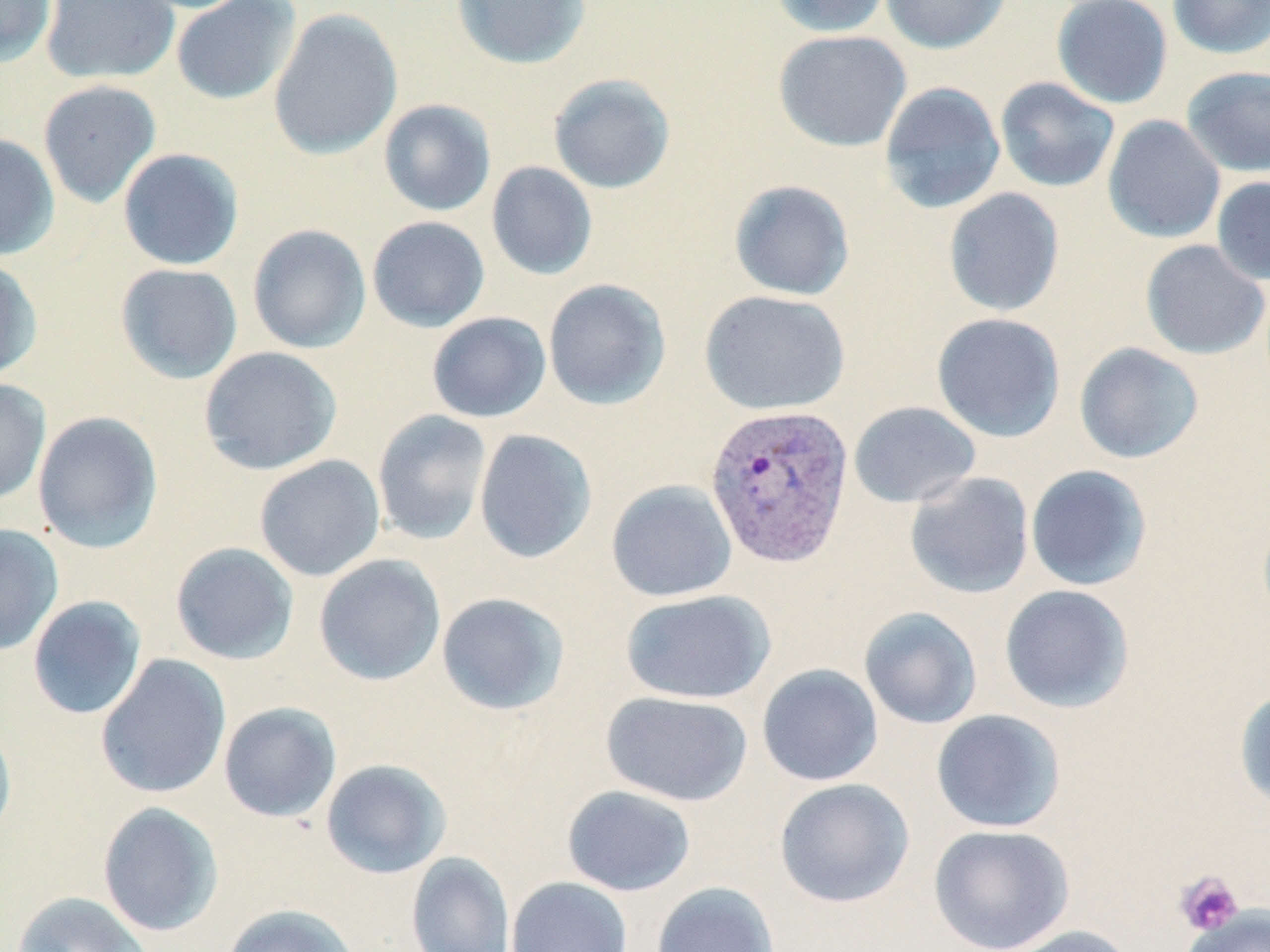

Summary:
  - Coordinate format: approximate bounding boxes as [x1, y1, x2, y2] in pixels
  - Plasmodium vivax-infected red blood cell locations: [704, 402, 855, 568]
  - Platelet locations: [1174, 870, 1244, 937]
  - Uninfected red blood cell locations: [0, 0, 58, 66], [40, 0, 179, 85], [171, 0, 302, 106], [451, 0, 591, 69], [770, 0, 892, 38], [881, 0, 1011, 54], [1051, 0, 1173, 109], [1168, 0, 1270, 59], [268, 8, 402, 160], [773, 30, 912, 152], [1181, 66, 1270, 177], [548, 74, 676, 194], [995, 77, 1120, 193], [37, 80, 162, 208], [878, 82, 1006, 214], [378, 99, 496, 217], [1103, 114, 1225, 244], [0, 132, 60, 261], [117, 148, 244, 270], [486, 161, 598, 280], [1211, 176, 1270, 285], [728, 180, 855, 301], [943, 187, 1065, 317], [367, 216, 490, 333], [247, 224, 371, 354], [1140, 240, 1269, 360], [0, 256, 42, 381], [115, 263, 243, 384], [543, 279, 672, 410], [699, 290, 849, 415], [426, 311, 551, 423], [932, 312, 1066, 442], [1074, 342, 1204, 464], [198, 346, 343, 475], [0, 379, 51, 506], [848, 401, 981, 508], [372, 410, 492, 546], [32, 411, 164, 553], [474, 428, 597, 564], [254, 454, 386, 582], [1025, 465, 1152, 591], [904, 472, 1034, 599], [606, 479, 738, 602], [0, 524, 64, 656], [169, 542, 299, 666], [313, 554, 446, 686], [999, 584, 1135, 713], [619, 589, 776, 705], [436, 592, 570, 715], [27, 595, 147, 720], [859, 607, 982, 729], [95, 654, 231, 799], [757, 664, 883, 787], [1233, 687, 1270, 811], [600, 690, 753, 806], [218, 702, 342, 823], [931, 709, 1066, 833], [0, 716, 17, 844], [320, 759, 451, 879], [773, 777, 915, 908], [562, 785, 697, 896], [98, 802, 224, 937], [928, 824, 1075, 952], [406, 852, 515, 952], [1173, 869, 1243, 938], [506, 876, 633, 952], [651, 881, 780, 952], [11, 891, 152, 952], [222, 903, 359, 952], [1182, 906, 1270, 952], [1002, 924, 1138, 952]
  - Slide-level diagnosis: Plasmodium vivax
  - Stain: May-Grünwald-Giemsa
  - Field of view: single
  - Magnification: 1000x
  - Preparation: thin blood film
  - Modality: light microscopy
  - Image size: 1270×952 pixels